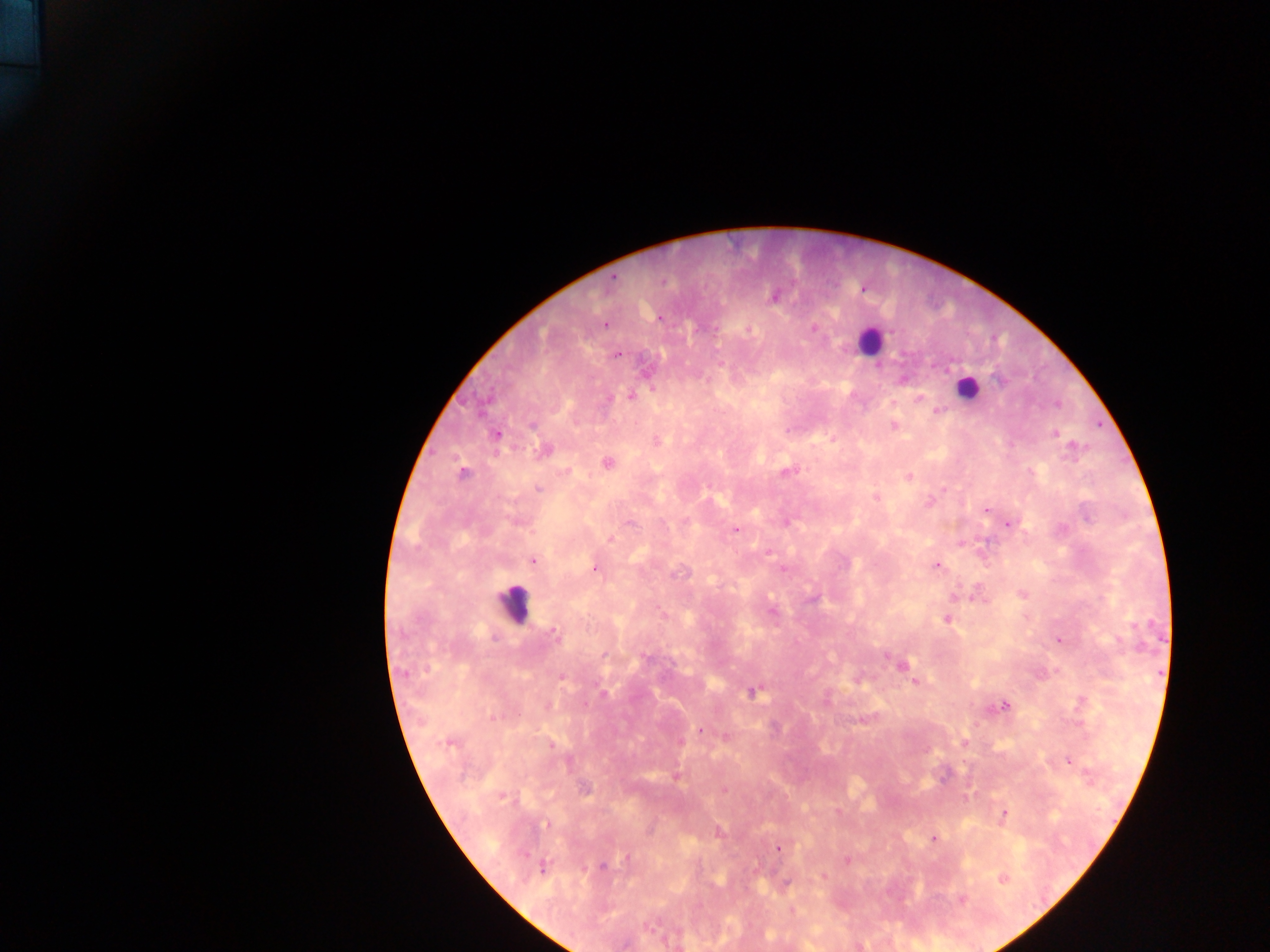

Approximate centers as x y in pixels.
Summary:
  - Leukocyte locations: 870 341; 966 388; 514 603
  - Malaria parasite locations: 614 277; 774 297; 660 318; 605 325; 814 327; 617 354; 1001 381; 631 395; 918 398; 1056 405; 936 411; 532 426; 894 426; 1054 433; 497 435; 656 442; 1073 445; 544 450; 607 463; 788 472; 462 474; 909 476; 538 489; 943 489; 876 498; 929 503; 986 509; 630 523; 1009 524; 735 529; 611 539; 769 552; 533 561; 937 565; 594 568; 783 570; 1022 594; 813 599; 772 612; 947 619; 554 635; 1059 641; 604 655; 886 655; 647 658; 901 665; 561 677; 915 681; 752 691; 603 693; 1082 700; 1004 705; 548 706; 493 717; 863 720; 700 730; 727 736; 681 742; 964 742; 448 744; 552 745; 1069 761; 676 777; 585 789; 725 789; 503 796; 838 811; 1002 814; 547 824; 933 838; 779 849; 629 857; 847 861; 602 866; 542 869; 1003 879; 786 883; 962 900
  - Field of view: single
  - Image size: 1270×952 pixels
  - Preparation: thick blood smear
  - Capture: mobile-phone photograph through a microscope
  - Country: Ghana